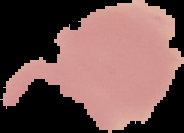
Summary:
  - Result: no Plasmodium parasites detected
  - Preparation: thin blood film
  - Image type: cell region segmented out of the field of view; surrounding area masked to black
  - Image size: 184×133 pixels